Give the extent of all Trypanosoma brucei.
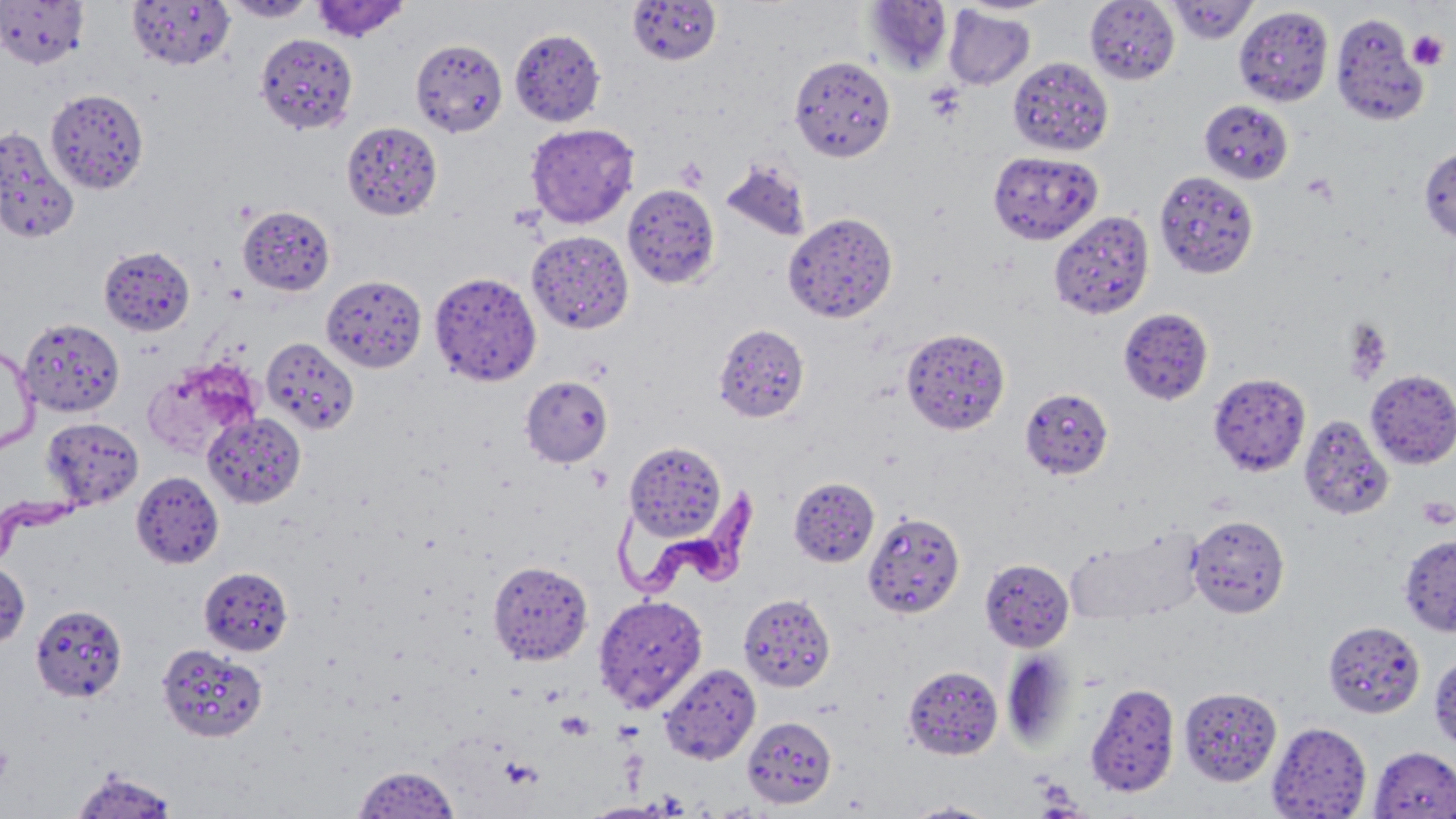

Approximate bounding boxes as (x1, y1, x2, y2) in pixels.
Trypanosoma brucei: (613, 482, 763, 603), (1, 483, 100, 557).

Summary:
  - Uninfected red blood cell locations: (0, 0, 90, 69), (127, 0, 236, 71), (220, 0, 320, 22), (311, 0, 410, 43), (627, 0, 723, 65), (956, 0, 1061, 16), (1084, 0, 1179, 85), (1167, 0, 1257, 44), (863, 2, 953, 74), (944, 5, 1036, 90), (1234, 5, 1333, 106), (1331, 13, 1429, 125), (510, 27, 605, 127), (253, 32, 359, 135), (410, 38, 508, 137), (789, 54, 895, 162), (1007, 56, 1114, 156), (45, 88, 149, 195), (1199, 99, 1294, 184), (341, 121, 443, 221), (525, 123, 639, 229), (0, 127, 79, 244), (1419, 147, 1456, 242), (988, 149, 1103, 244), (720, 159, 811, 243), (1154, 168, 1260, 277), (623, 184, 721, 289), (238, 205, 335, 295), (1048, 209, 1155, 321), (787, 212, 902, 323), (526, 230, 633, 334), (99, 246, 195, 335), (440, 273, 544, 381), (321, 276, 427, 372), (1119, 309, 1213, 406), (19, 317, 125, 417), (713, 323, 809, 422), (900, 327, 1010, 435), (261, 337, 359, 434), (0, 343, 38, 457), (143, 358, 261, 460), (1365, 369, 1456, 469), (1208, 372, 1311, 476), (520, 375, 613, 467), (1020, 387, 1114, 479), (203, 412, 306, 509), (1298, 413, 1394, 521), (41, 417, 144, 510), (625, 441, 726, 541), (131, 470, 224, 568), (789, 477, 879, 567), (862, 510, 965, 619), (1187, 514, 1290, 618), (1065, 529, 1202, 624), (1399, 534, 1456, 635), (980, 558, 1075, 652), (0, 560, 30, 650), (488, 560, 593, 665), (198, 566, 293, 656), (739, 593, 835, 692), (594, 594, 708, 712), (30, 604, 127, 702), (1323, 620, 1424, 719), (156, 642, 267, 742), (1001, 651, 1076, 750), (1429, 654, 1456, 752), (660, 663, 761, 765), (903, 665, 1002, 759), (1086, 682, 1180, 798), (1179, 686, 1281, 785), (742, 715, 837, 808), (1267, 722, 1371, 818), (1369, 746, 1456, 819), (352, 765, 461, 817), (69, 768, 181, 818), (900, 800, 1003, 818)
  - Platelet locations: (1408, 30, 1448, 71), (674, 157, 709, 191), (1345, 320, 1392, 384), (1417, 496, 1455, 529), (0, 742, 15, 787)
  - Slide-level diagnosis: Trypanosoma brucei
  - Field of view: one of a larger specimen
  - Preparation: thin blood film
  - Image size: 1456×819 pixels
  - Stain: May-Grünwald-Giemsa
  - Modality: light microscopy
  - Magnification: 1000x